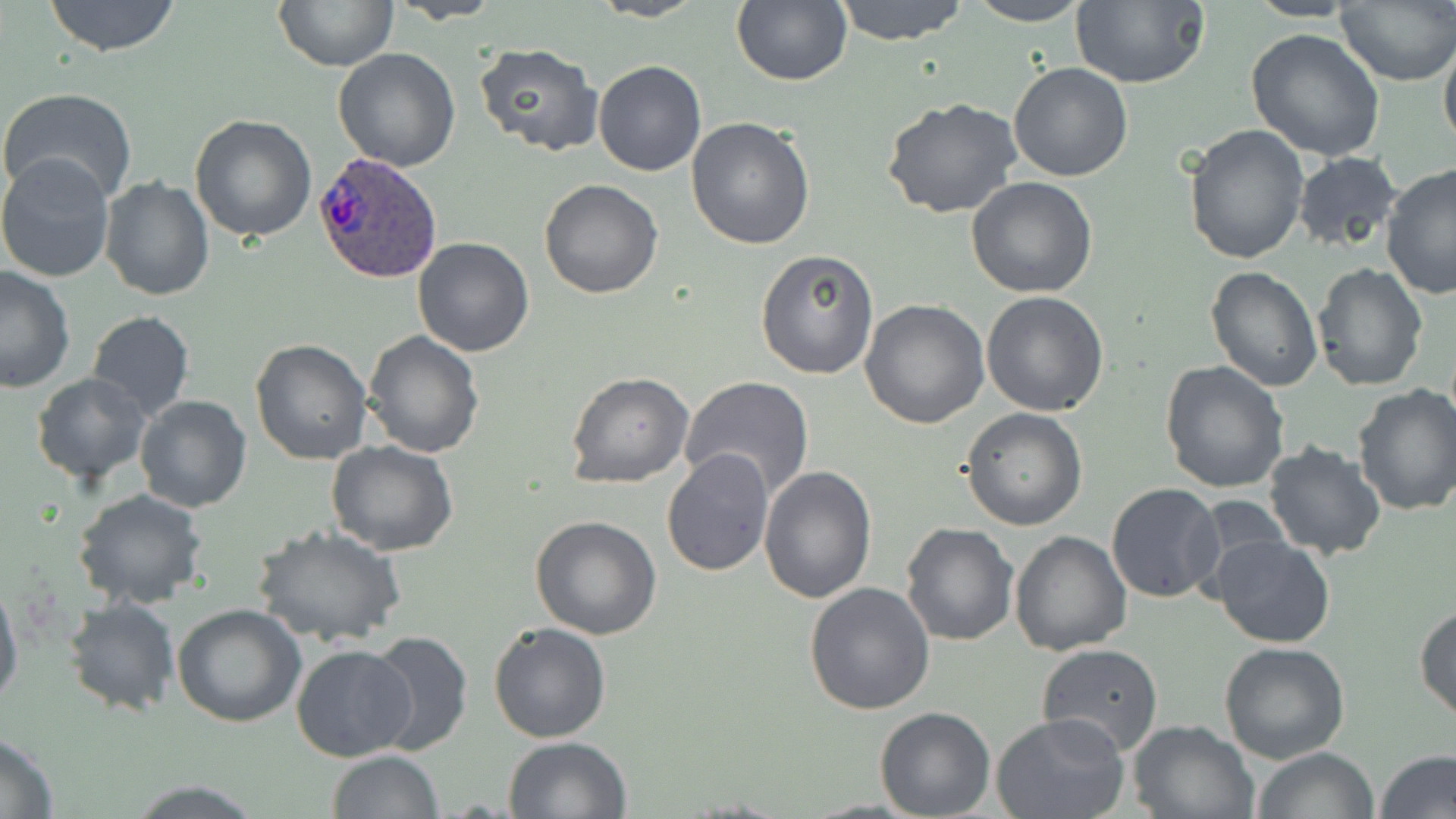
Approximate bounding boxes as [x1, y1, x2, y2] in pixels. Uninfected red blood cell locations: [43, 0, 183, 56], [588, 0, 708, 23], [732, 0, 852, 86], [832, 0, 969, 45], [1069, 0, 1209, 89], [273, 1, 399, 70], [390, 1, 504, 23], [964, 1, 1093, 26], [1336, 2, 1456, 86], [1244, 27, 1388, 161], [1439, 30, 1456, 159], [473, 43, 603, 155], [332, 49, 461, 171], [592, 61, 707, 177], [1007, 62, 1134, 182], [1, 86, 138, 207], [881, 97, 1026, 221], [189, 114, 317, 243], [687, 116, 816, 250], [1184, 125, 1310, 267], [1291, 151, 1405, 257], [0, 152, 118, 284], [1379, 163, 1455, 300], [965, 175, 1098, 298], [100, 176, 214, 302], [539, 179, 665, 298], [411, 237, 536, 357], [755, 247, 879, 380], [1311, 261, 1429, 392], [0, 264, 77, 394], [1205, 266, 1323, 392], [980, 291, 1109, 415], [858, 298, 990, 430], [86, 310, 195, 423], [363, 331, 485, 459], [250, 338, 374, 465], [1158, 360, 1289, 494], [567, 372, 694, 488], [31, 373, 152, 486], [680, 376, 816, 501], [1351, 383, 1456, 518], [135, 394, 252, 512], [960, 409, 1087, 530], [324, 439, 458, 556], [1262, 439, 1388, 561], [662, 449, 774, 576], [759, 466, 877, 604], [1105, 483, 1225, 604], [70, 489, 209, 609], [531, 516, 663, 639], [900, 522, 1019, 645], [251, 524, 406, 647], [1008, 531, 1132, 655], [1209, 534, 1335, 649], [0, 576, 23, 714], [804, 583, 935, 717], [63, 597, 180, 716], [171, 603, 306, 727], [1414, 604, 1456, 725], [488, 622, 611, 743], [364, 631, 473, 756], [1037, 642, 1165, 756], [1219, 643, 1350, 765], [291, 644, 417, 763], [874, 707, 996, 819], [992, 713, 1131, 819], [1127, 718, 1258, 818], [0, 733, 59, 816], [502, 736, 631, 818], [1250, 747, 1380, 819], [326, 750, 442, 818], [1376, 750, 1456, 819], [125, 780, 265, 816]. Plasmodium ovale-infected red blood cell locations: [314, 150, 442, 284]. Slide-level diagnosis: Plasmodium ovale. May-Grünwald-Giemsa stain. One field of a larger specimen. Image is 1456×819 pixels. Captured at 1000x magnification. Light microscopy. Thin blood smear.